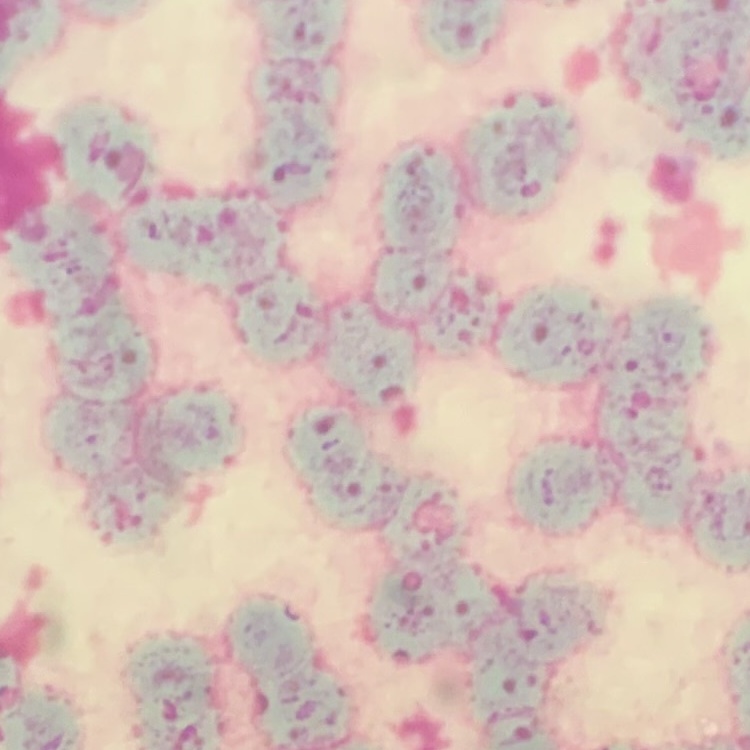

erythrocyte morphology = rouleaux formation
stain = Field's or Giemsa
preparation = thin blood smear
image type = square crop of a larger photomicrograph